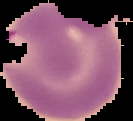 Malaria status: parasitized. Cell region segmented out of the field of view; the surrounding area is masked to black. Image is 133×121 pixels. From a thin blood smear.